State which cell type is depicted.
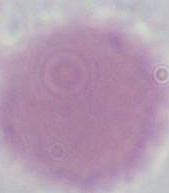

This is an erythrocyte.

Photomicrograph. Captured at 1000x magnification.